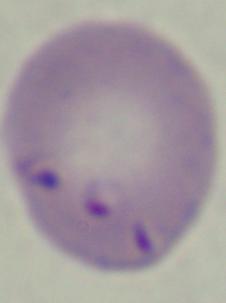

Summary:
  - Identification: Babesia
  - Modality: photomicrograph
  - Magnification: 1000x